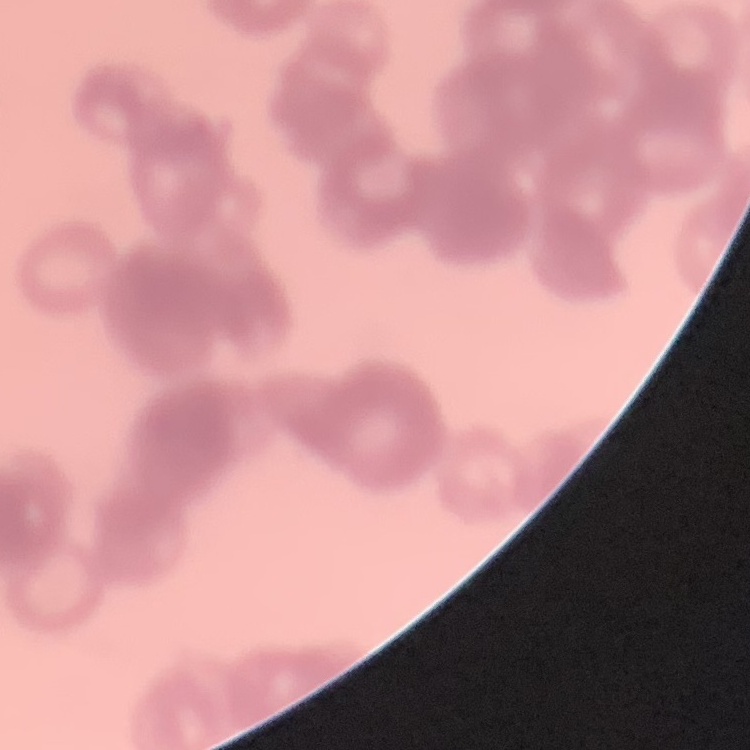
red blood cell morphology = rouleaux formation
preparation = thin blood smear
stain = Field's or Giemsa
image type = one tile cut from a larger photomicrograph